Locate and identify every blood parasite.
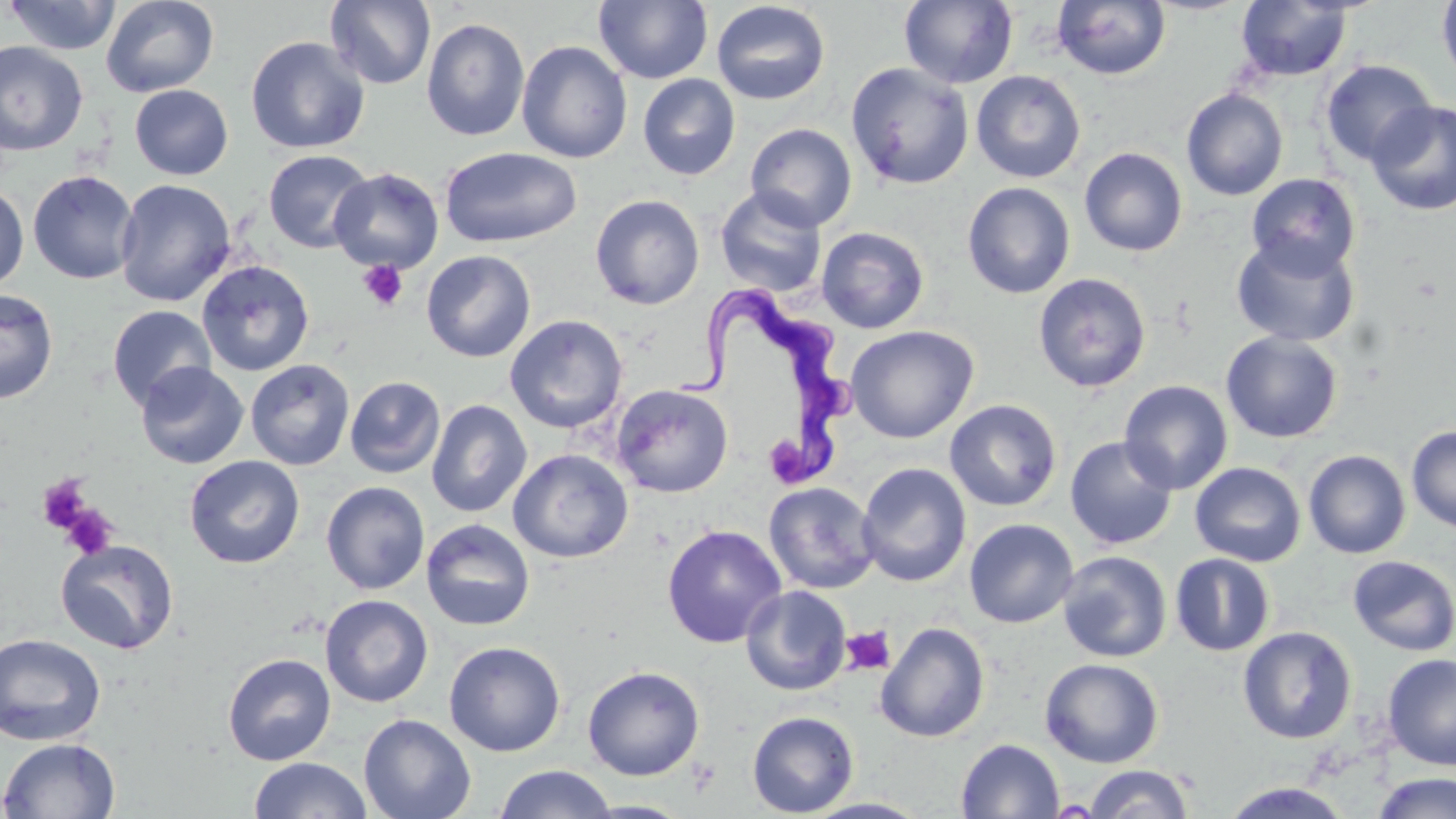
Approximate bounding boxes as (x1, y1, x2, y2) in pixels.
Trypanosoma brucei: (674, 286, 857, 482).
No Plasmodium falciparum, Plasmodium ovale, Plasmodium malariae, Plasmodium vivax, or Babesia divergens observed.

Uninfected red blood cell locations: (4, 0, 122, 55), (100, 0, 220, 98), (325, 0, 435, 89), (594, 0, 713, 84), (1437, 0, 1456, 89), (711, 1, 831, 106), (899, 1, 1018, 89), (1052, 1, 1171, 81), (1235, 1, 1353, 81), (421, 17, 530, 142), (246, 36, 370, 154), (0, 41, 88, 156), (517, 41, 632, 163), (1321, 60, 1436, 167), (845, 62, 974, 190), (971, 70, 1086, 183), (637, 73, 741, 180), (129, 85, 233, 180), (1181, 88, 1288, 200), (1367, 100, 1456, 215), (745, 123, 857, 232), (439, 147, 582, 248), (1079, 147, 1188, 256), (263, 150, 374, 254), (329, 168, 444, 274), (27, 170, 139, 285), (1246, 173, 1361, 279), (114, 179, 236, 307), (962, 181, 1076, 299), (0, 184, 29, 290), (715, 187, 827, 297), (590, 194, 705, 309), (816, 226, 929, 333), (1230, 234, 1360, 347), (422, 250, 536, 362), (196, 260, 314, 376), (1033, 272, 1152, 393), (0, 288, 58, 404), (107, 305, 216, 409), (504, 315, 628, 434), (845, 325, 979, 443), (1220, 331, 1343, 444), (245, 359, 355, 470), (135, 361, 249, 469), (345, 376, 445, 478), (1119, 380, 1233, 495), (611, 384, 733, 498), (426, 399, 532, 518), (944, 399, 1062, 511), (1406, 426, 1456, 533), (1065, 436, 1177, 550), (508, 449, 634, 563), (1303, 449, 1411, 559), (184, 455, 305, 569), (857, 462, 972, 587), (1190, 462, 1306, 567), (321, 481, 430, 595), (764, 481, 880, 594), (421, 518, 536, 631), (964, 518, 1079, 628), (662, 524, 787, 648), (55, 538, 180, 655), (1057, 551, 1172, 662), (1170, 553, 1276, 656), (1348, 555, 1456, 656), (740, 585, 851, 696), (320, 594, 434, 707), (876, 622, 990, 743), (1238, 626, 1356, 744), (0, 633, 106, 746), (444, 641, 566, 757), (222, 653, 336, 766), (1381, 653, 1456, 771), (1040, 658, 1164, 768), (582, 666, 705, 780), (747, 710, 859, 817), (358, 713, 476, 819), (0, 738, 120, 819), (956, 738, 1064, 819), (248, 756, 372, 818), (1084, 764, 1195, 819), (494, 765, 617, 819), (1370, 773, 1456, 819), (1221, 782, 1352, 818), (802, 797, 932, 818), (579, 800, 695, 818). Platelet locations: (357, 259, 408, 312), (770, 439, 811, 481), (37, 475, 93, 533), (59, 503, 119, 560), (841, 625, 896, 676). Slide-level diagnosis: Trypanosoma brucei. Light microscopy. Single field of view. Thin blood film. Image is 1456×819 pixels. May-Grünwald-Giemsa-stained preparation. 1000x magnification.